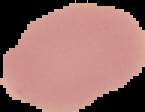
Malaria status: uninfected. From a thin blood film. Segmented cell region on a black background. Image is 145×112 pixels.